Name the parasite shown.
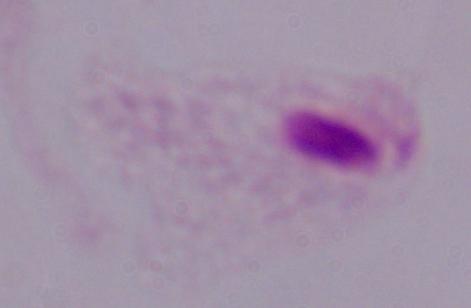
This is a trichomonad.

Summary:
  - Modality: micrograph
  - Magnification: 1000x